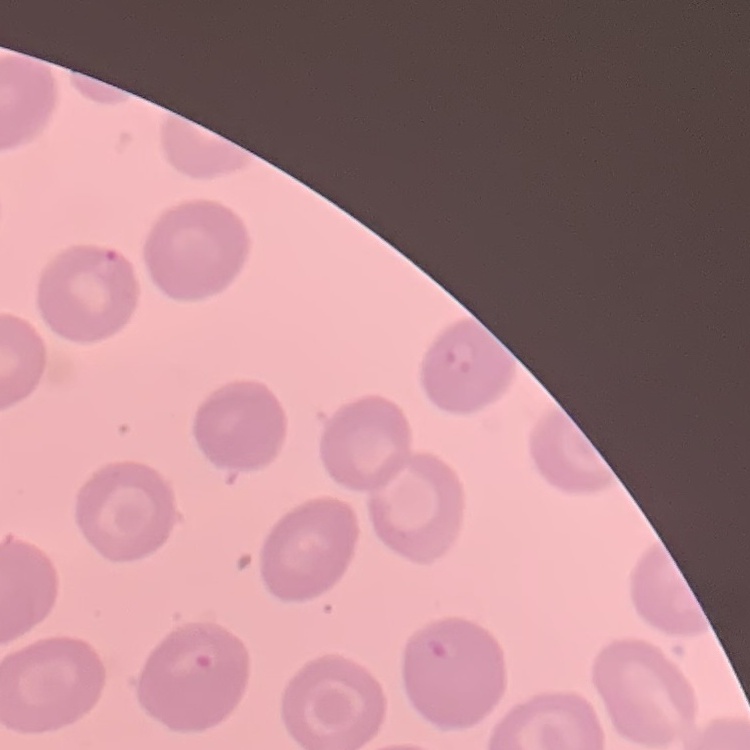

red blood cell morphology = no rouleaux formation
stain = Field's or Giemsa
image type = square crop of a larger photomicrograph
preparation = thin blood smear